Name the parasite shown.
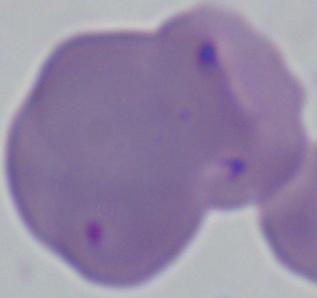

Babesia.

magnification: 1000x
modality: photomicrograph